Look for Plasmodium parasites.
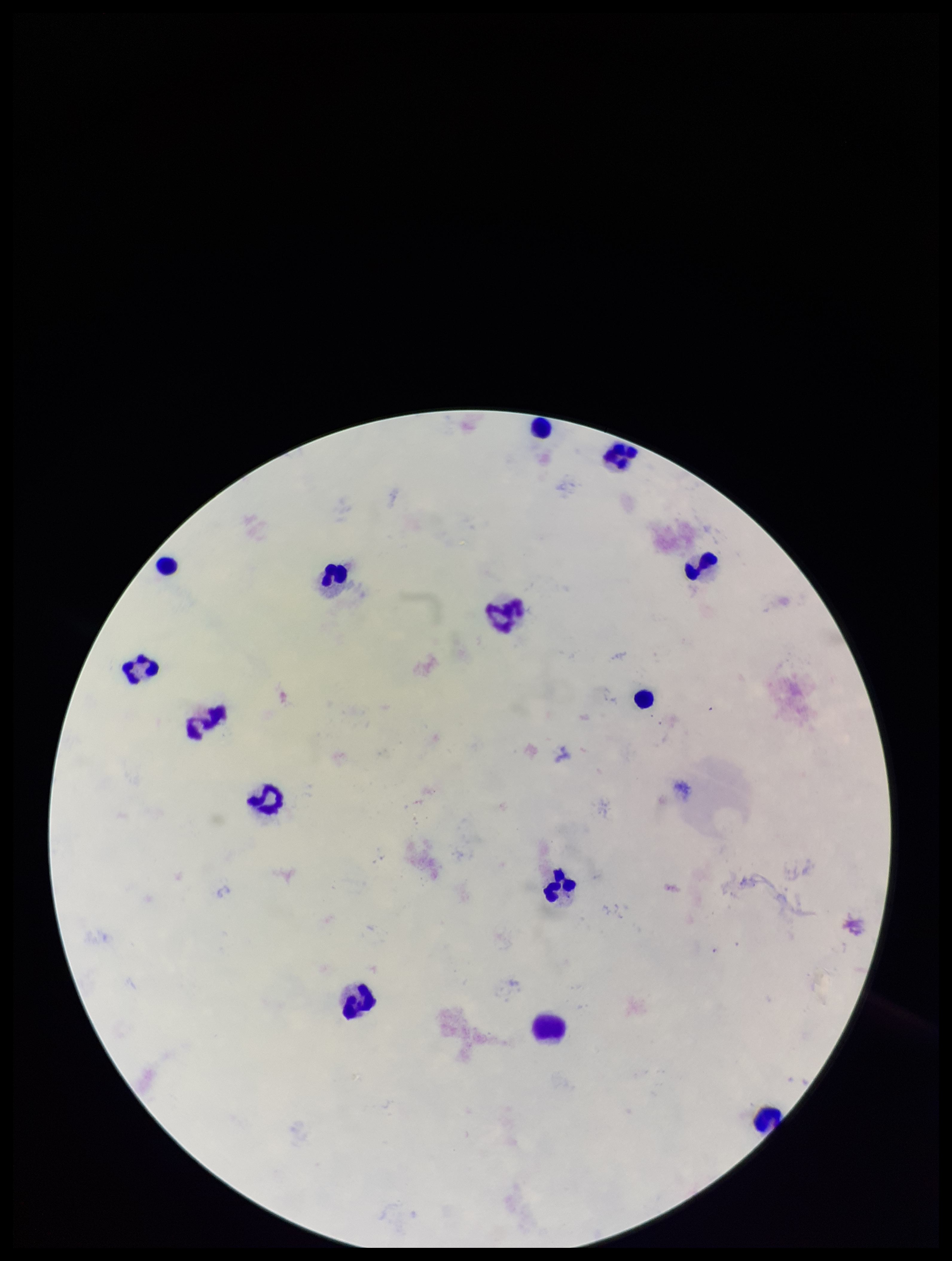

None identified.

parasite count = 0
stain = Giemsa
capture = smartphone photograph through the microscope eyepiece
leukocyte count = 14
patient malaria status = negative
field of view = single
image size = 952×1261 pixels
preparation = thick smear